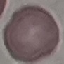 Result: negative for malaria parasites. Giemsa stain. Cell patch, automatically extracted from a larger field of view and resized to 64 × 64 pixels. Photographed with a smartphone camera at the microscope eyepiece. Thin blood film.